Classify this cell by malaria status.
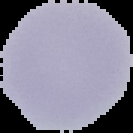

It is uninfected.

image type = segmented cell region on a black background
image size = 133×133 pixels
preparation = thin blood smear